Assess this cell for malaria.
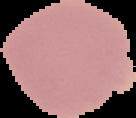
Uninfected.

From a thin blood smear. Image is 136×118 pixels. The area outside the segmented cell region is set to black.